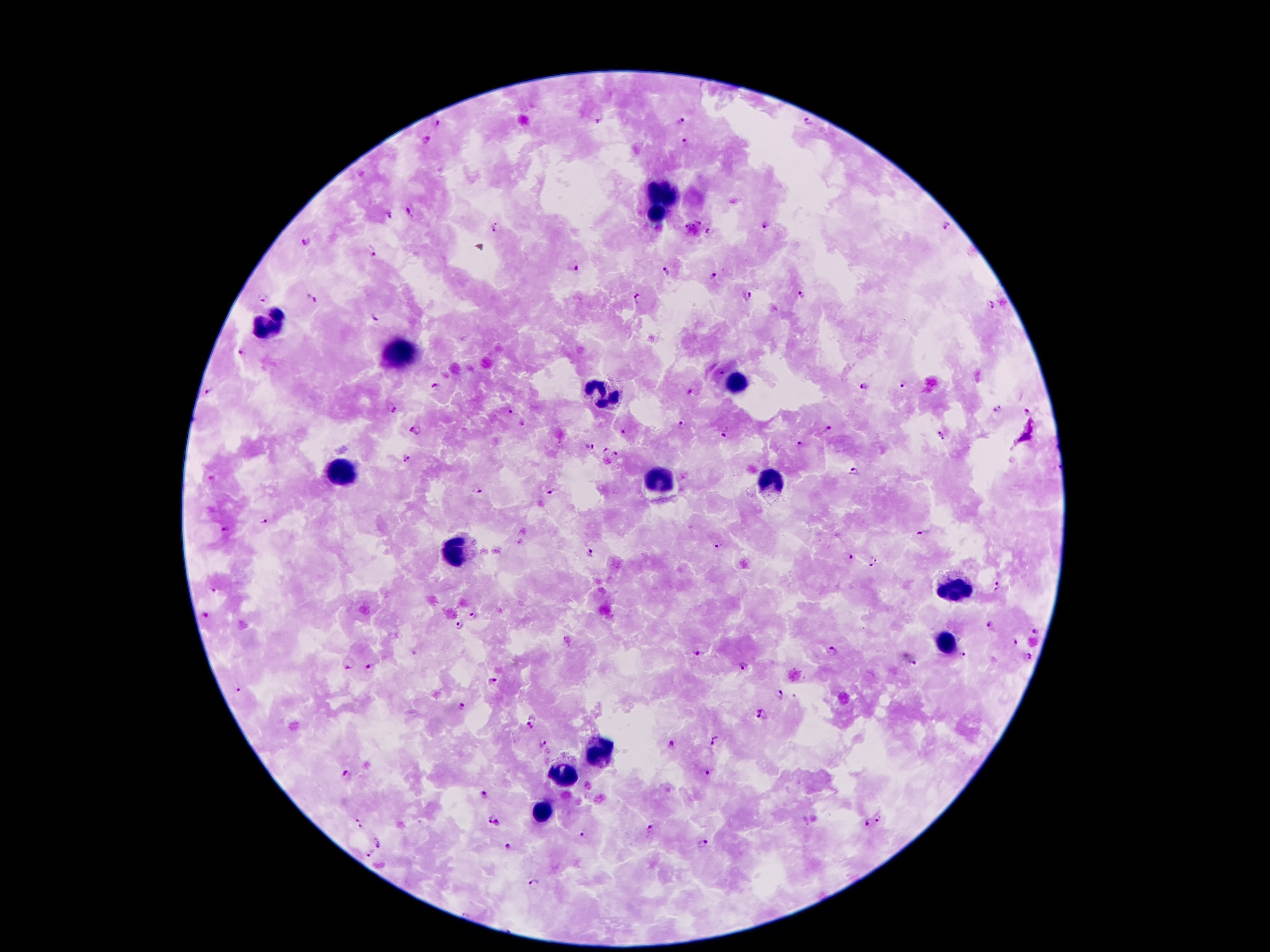

{
  "malaria_parasite_locations": "approximate object centers, in pixels from the top-left corner: (x=597, y=118), (x=682, y=121), (x=436, y=122), (x=808, y=122), (x=424, y=141), (x=684, y=141), (x=409, y=210), (x=389, y=214), (x=768, y=224), (x=947, y=225), (x=496, y=227), (x=693, y=229), (x=709, y=232), (x=308, y=240), (x=371, y=251), (x=574, y=265), (x=666, y=272), (x=712, y=276), (x=802, y=294), (x=745, y=295), (x=263, y=297), (x=311, y=298), (x=637, y=299), (x=993, y=305), (x=376, y=316), (x=242, y=351), (x=720, y=372), (x=905, y=383), (x=435, y=385), (x=864, y=386), (x=211, y=389), (x=389, y=409), (x=996, y=410), (x=511, y=412), (x=1025, y=412), (x=681, y=424), (x=828, y=430), (x=415, y=431), (x=625, y=432), (x=726, y=433), (x=940, y=434), (x=800, y=444), (x=589, y=445), (x=606, y=451), (x=615, y=455), (x=405, y=460), (x=607, y=461), (x=854, y=472), (x=478, y=491), (x=551, y=492), (x=265, y=523), (x=225, y=529), (x=923, y=532), (x=718, y=545), (x=589, y=554), (x=848, y=557), (x=874, y=562), (x=997, y=587), (x=212, y=592), (x=474, y=615), (x=205, y=616), (x=990, y=624), (x=461, y=626), (x=1037, y=630), (x=1013, y=640), (x=831, y=651), (x=698, y=654), (x=964, y=655), (x=1028, y=657), (x=915, y=662), (x=349, y=665), (x=743, y=666), (x=370, y=667), (x=493, y=680), (x=237, y=689), (x=781, y=694), (x=462, y=707), (x=764, y=713), (x=531, y=719), (x=542, y=742), (x=712, y=742), (x=672, y=744), (x=707, y=772), (x=344, y=774), (x=486, y=795), (x=487, y=818), (x=880, y=820), (x=867, y=823), (x=358, y=824), (x=650, y=830), (x=584, y=835), (x=703, y=843), (x=379, y=845), (x=508, y=847), (x=371, y=853), (x=534, y=883)",
  "capture": "smartphone through the microscope eyepiece",
  "field_of_view": "one from this slide",
  "leukocyte_locations": "approximate object centers, in pixels from the top-left corner: (x=664, y=194), (x=655, y=217), (x=268, y=323), (x=399, y=351), (x=735, y=382), (x=598, y=395), (x=343, y=475), (x=657, y=482), (x=768, y=483), (x=456, y=550), (x=960, y=591), (x=947, y=644), (x=591, y=751), (x=560, y=778), (x=540, y=813)",
  "preparation": "thick blood smear",
  "stain": "Giemsa",
  "image_size": "1270×952 pixels",
  "patient_malaria_status": "infected with Plasmodium falciparum",
  "magnification": "100x"
}